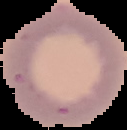
Summary:
  - Result: negative for malaria parasites
  - Image type: segmented cell region on a black background
  - Image size: 127×130 pixels
  - Preparation: thin blood film